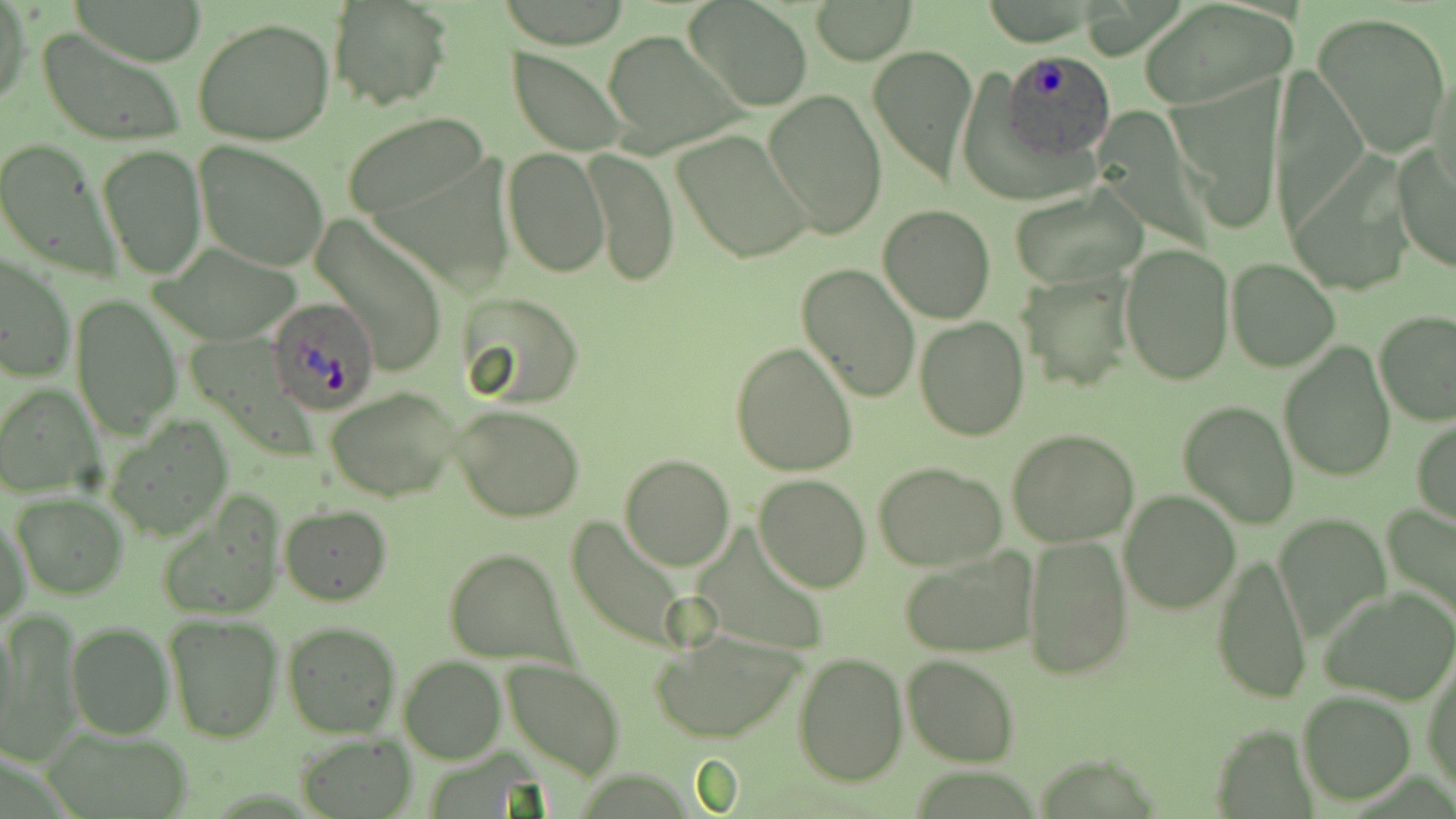

Approximate bounding boxes as (x1,y1)-(x2,y2) corner pairs in pixels. Uninfected red blood cell locations: (67,0)-(210,66), (329,1)-(452,112), (686,2)-(812,112), (812,2)-(914,64), (1139,2)-(1298,109), (0,3)-(29,109), (1312,13)-(1451,157), (191,16)-(338,147), (37,26)-(187,147), (602,30)-(744,154), (867,43)-(978,185), (509,46)-(630,156), (1429,64)-(1455,196), (1169,88)-(1283,233), (762,90)-(887,239), (341,111)-(491,220), (672,129)-(815,265), (1,137)-(120,280), (194,141)-(331,270), (1392,142)-(1456,274), (96,143)-(207,281), (588,147)-(678,286), (501,148)-(609,279), (1288,154)-(1423,298), (1010,183)-(1148,290), (877,204)-(996,323), (312,215)-(451,379), (152,243)-(305,342), (1119,243)-(1234,385), (1,252)-(75,384), (1225,256)-(1340,371), (796,263)-(922,404), (1018,273)-(1134,393), (458,291)-(586,405), (70,293)-(182,439), (1375,310)-(1456,426), (914,317)-(1029,442), (1278,341)-(1397,483), (731,342)-(858,478), (0,383)-(102,497), (324,386)-(463,502), (1178,400)-(1300,529), (452,404)-(585,521), (105,417)-(234,543), (1412,418)-(1456,526), (1007,428)-(1139,547), (618,454)-(737,572), (874,461)-(1006,569), (752,473)-(872,592), (1119,491)-(1240,614), (10,492)-(128,600), (154,498)-(282,622), (279,504)-(392,605), (1383,508)-(1455,627), (1,509)-(30,628), (1276,512)-(1390,641), (565,516)-(694,652), (1023,536)-(1132,678), (444,546)-(572,668), (900,547)-(1038,660), (1210,551)-(1312,703), (1323,587)-(1455,704), (163,613)-(284,743), (4,616)-(80,757), (0,617)-(21,751), (66,620)-(173,739), (280,620)-(402,739), (650,628)-(807,743), (791,651)-(907,786), (902,653)-(1019,767), (1424,653)-(1455,800), (399,656)-(505,763), (500,659)-(626,779), (1297,689)-(1416,805), (40,725)-(198,819), (295,736)-(418,817). Plasmodium ovale-infected red blood cell locations: (1001,48)-(1117,162), (267,296)-(379,416). Slide-level diagnosis: Plasmodium ovale. Image is 1456×819 pixels. Optical microscopy. Single field of view. 1000x magnification. Thin blood smear. May-Grünwald-Giemsa stain.